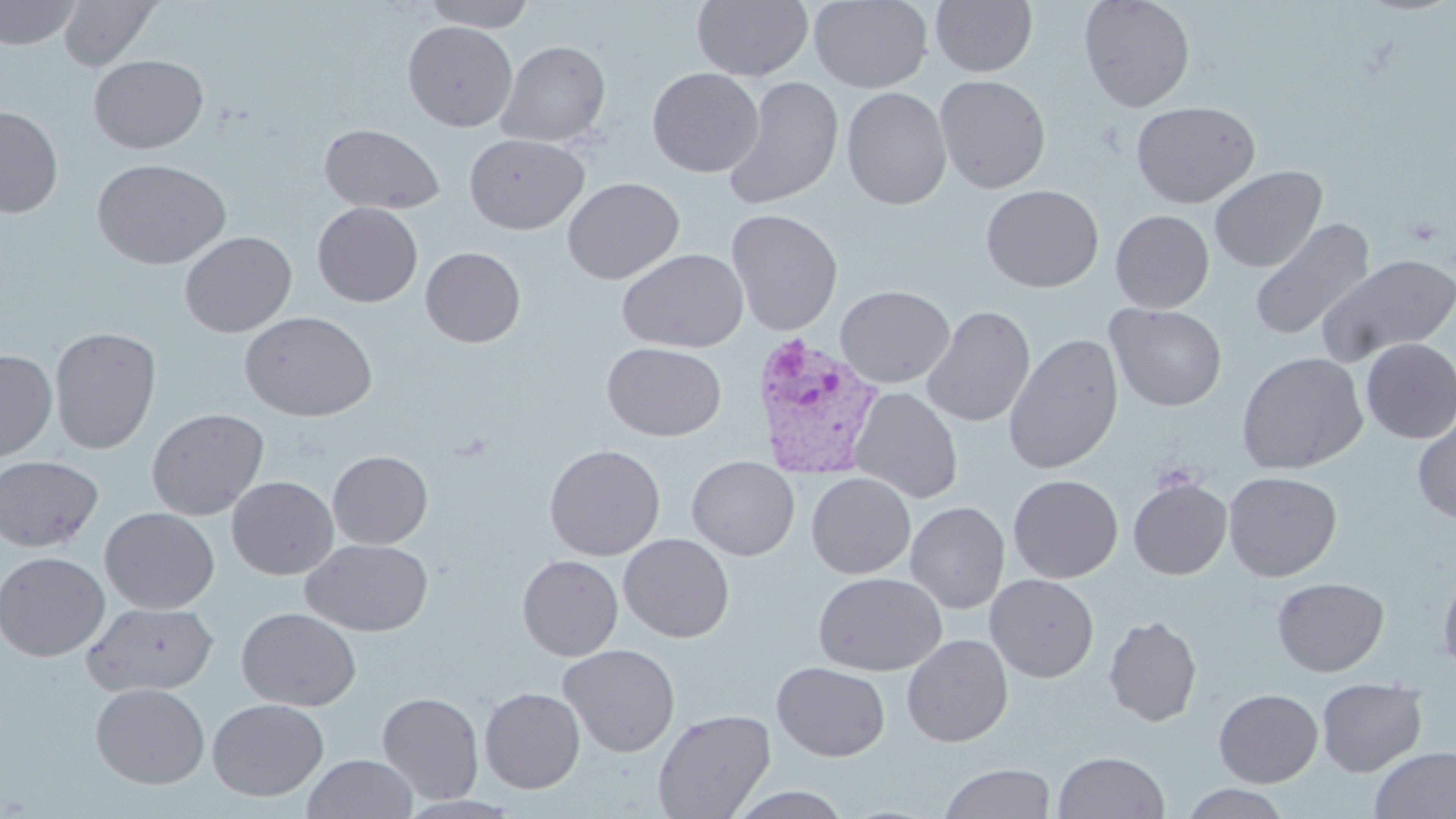
Summary:
  - Coordinate format: approximate bounding boxes as named x1/y1/x2/y2 corners in pixels
  - Plasmodium vivax-infected red blood cell locations: (x1=749, y1=333, x2=885, y2=480)
  - Uninfected red blood cell locations: (x1=0, y1=0, x2=81, y2=49), (x1=58, y1=0, x2=163, y2=71), (x1=419, y1=0, x2=536, y2=30), (x1=692, y1=0, x2=813, y2=82), (x1=809, y1=0, x2=932, y2=92), (x1=930, y1=0, x2=1038, y2=77), (x1=1078, y1=0, x2=1195, y2=112), (x1=403, y1=20, x2=518, y2=131), (x1=496, y1=40, x2=611, y2=147), (x1=88, y1=54, x2=209, y2=154), (x1=647, y1=67, x2=764, y2=178), (x1=934, y1=74, x2=1051, y2=194), (x1=721, y1=76, x2=844, y2=211), (x1=842, y1=87, x2=952, y2=210), (x1=1131, y1=101, x2=1260, y2=208), (x1=0, y1=106, x2=63, y2=218), (x1=318, y1=124, x2=444, y2=213), (x1=465, y1=134, x2=589, y2=234), (x1=92, y1=158, x2=230, y2=269), (x1=1209, y1=165, x2=1327, y2=273), (x1=562, y1=177, x2=685, y2=284), (x1=981, y1=184, x2=1104, y2=292), (x1=313, y1=202, x2=423, y2=307), (x1=725, y1=208, x2=843, y2=337), (x1=1110, y1=210, x2=1214, y2=313), (x1=1249, y1=218, x2=1374, y2=342), (x1=179, y1=231, x2=297, y2=337), (x1=420, y1=246, x2=526, y2=347), (x1=617, y1=248, x2=748, y2=352), (x1=1318, y1=253, x2=1456, y2=365), (x1=836, y1=285, x2=955, y2=388), (x1=1107, y1=303, x2=1227, y2=412), (x1=921, y1=305, x2=1035, y2=427), (x1=239, y1=311, x2=377, y2=422), (x1=49, y1=326, x2=161, y2=454), (x1=1003, y1=333, x2=1124, y2=475), (x1=1360, y1=338, x2=1456, y2=444), (x1=602, y1=342, x2=727, y2=441), (x1=0, y1=349, x2=57, y2=461), (x1=1236, y1=351, x2=1368, y2=475), (x1=850, y1=387, x2=963, y2=503), (x1=146, y1=408, x2=269, y2=521), (x1=1412, y1=412, x2=1456, y2=525), (x1=544, y1=443, x2=665, y2=560), (x1=328, y1=451, x2=433, y2=549), (x1=0, y1=455, x2=102, y2=551), (x1=686, y1=456, x2=799, y2=561), (x1=1223, y1=471, x2=1342, y2=582), (x1=806, y1=473, x2=916, y2=578), (x1=1008, y1=475, x2=1123, y2=582), (x1=227, y1=476, x2=338, y2=579), (x1=1128, y1=477, x2=1232, y2=580), (x1=906, y1=501, x2=1010, y2=613), (x1=100, y1=507, x2=219, y2=614), (x1=618, y1=533, x2=735, y2=642), (x1=300, y1=539, x2=434, y2=636), (x1=0, y1=551, x2=110, y2=661), (x1=517, y1=555, x2=623, y2=660), (x1=1437, y1=565, x2=1456, y2=675), (x1=813, y1=572, x2=947, y2=676), (x1=985, y1=574, x2=1099, y2=682), (x1=1272, y1=577, x2=1389, y2=677), (x1=82, y1=601, x2=218, y2=697), (x1=236, y1=607, x2=361, y2=711), (x1=1103, y1=615, x2=1202, y2=727), (x1=902, y1=634, x2=1013, y2=746), (x1=558, y1=644, x2=680, y2=756), (x1=772, y1=662, x2=890, y2=761), (x1=1316, y1=677, x2=1427, y2=777), (x1=90, y1=682, x2=210, y2=788), (x1=479, y1=687, x2=585, y2=793), (x1=1214, y1=688, x2=1323, y2=787), (x1=377, y1=691, x2=484, y2=804), (x1=208, y1=698, x2=329, y2=801), (x1=653, y1=708, x2=776, y2=819), (x1=1370, y1=746, x2=1456, y2=819), (x1=1053, y1=750, x2=1170, y2=818), (x1=302, y1=754, x2=418, y2=819), (x1=939, y1=763, x2=1056, y2=819), (x1=1178, y1=784, x2=1293, y2=819), (x1=726, y1=786, x2=855, y2=819)
  - Slide-level diagnosis: Plasmodium vivax
  - Magnification: 1000x
  - Preparation: thin blood film
  - Field of view: one of a larger specimen
  - Image size: 1456×819 pixels
  - Modality: light microscopy
  - Stain: May-Grünwald-Giemsa